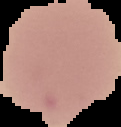

From a thin blood smear. Cell region segmented out of the field of view; the surrounding area is masked to black. Malaria status: uninfected. Image is 121×127 pixels.